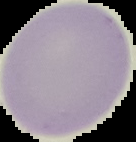
Summary:
  - Image type: segmented cell region with the area outside set to black
  - Image size: 136×142 pixels
  - Malaria status: uninfected
  - Preparation: thin blood smear